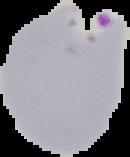
image_type: segmented cell region with the area outside set to black
image_size: 130×157 pixels
preparation: thin blood film
malaria_status: parasitized